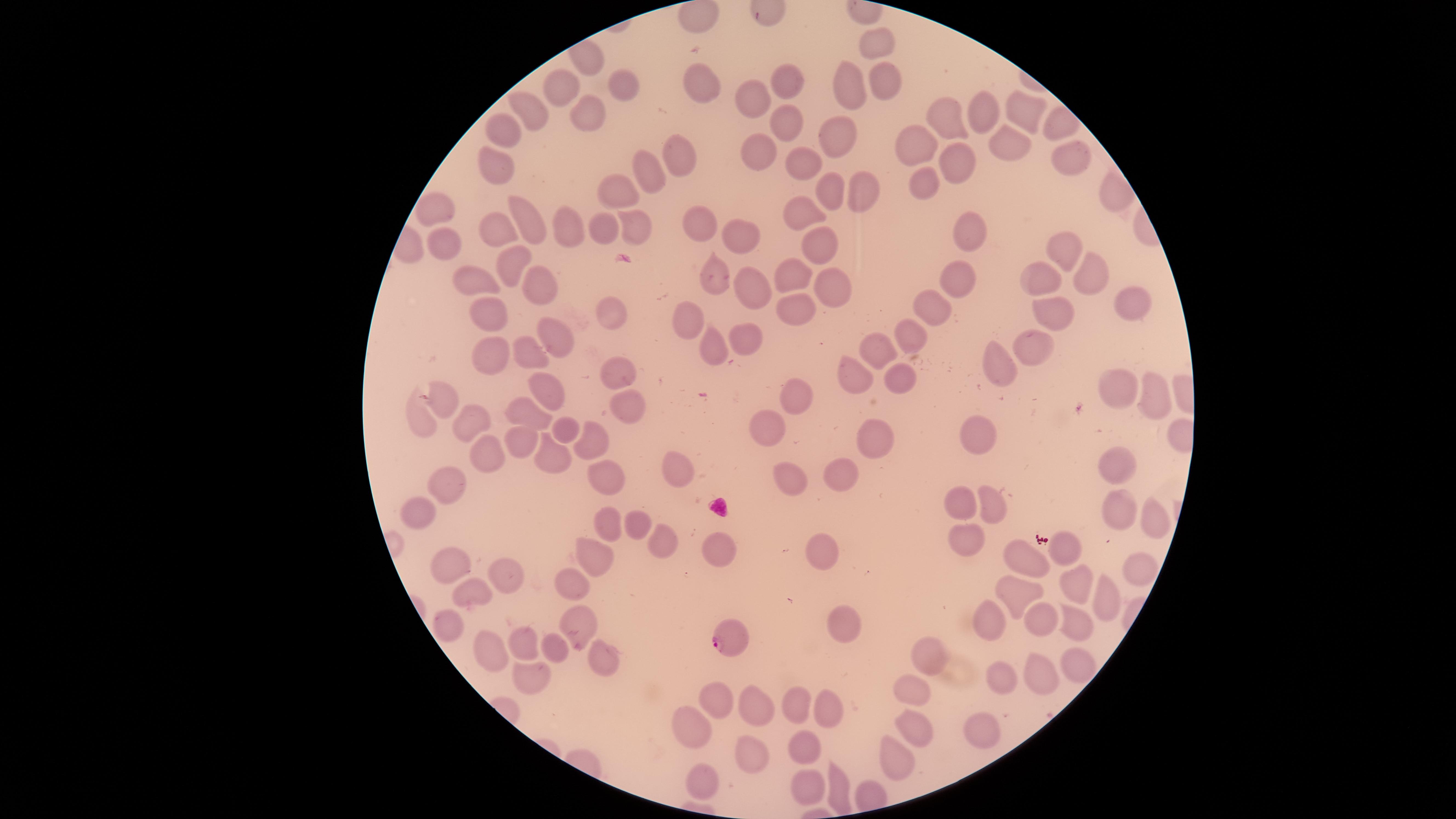
stain = Giemsa
preparation = thin blood film
parasitized red blood cells = approximate marker points, in pixels from the top-left corner: (x=734, y=638)
visible region = circular
capture = smartphone photograph through the microscope eyepiece
field of view = single
presence = malaria parasites identified
species = Plasmodium falciparum
uninfected red blood cells = approximate marker points, in pixels from the top-left corner: (x=701, y=14), (x=880, y=36), (x=789, y=76), (x=882, y=79), (x=570, y=80), (x=703, y=83), (x=849, y=83), (x=626, y=84), (x=750, y=100), (x=535, y=104), (x=581, y=111), (x=986, y=111), (x=1030, y=112), (x=957, y=118), (x=783, y=126), (x=506, y=129), (x=835, y=132), (x=915, y=142), (x=1004, y=143), (x=684, y=152), (x=758, y=152), (x=799, y=156), (x=493, y=158), (x=953, y=165), (x=649, y=176), (x=921, y=179), (x=825, y=185), (x=860, y=185), (x=616, y=192), (x=436, y=202), (x=805, y=210), (x=528, y=212), (x=702, y=223), (x=570, y=224), (x=602, y=229), (x=631, y=231), (x=500, y=234), (x=739, y=236), (x=976, y=236), (x=444, y=237), (x=1063, y=244), (x=819, y=245), (x=508, y=260), (x=1086, y=265), (x=713, y=267), (x=791, y=273), (x=484, y=278), (x=965, y=278), (x=1046, y=279), (x=830, y=281), (x=535, y=286), (x=748, y=292), (x=1132, y=306), (x=793, y=307), (x=611, y=309), (x=936, y=310), (x=1052, y=315), (x=495, y=318), (x=693, y=323), (x=912, y=333), (x=743, y=335), (x=555, y=338), (x=1031, y=341), (x=879, y=344), (x=531, y=348), (x=717, y=348), (x=489, y=358), (x=993, y=365), (x=897, y=371), (x=621, y=375), (x=857, y=375), (x=547, y=386), (x=1119, y=386), (x=796, y=388), (x=443, y=390), (x=1157, y=395), (x=625, y=408), (x=424, y=412), (x=533, y=415), (x=471, y=428), (x=569, y=428), (x=766, y=428), (x=594, y=429), (x=973, y=431), (x=874, y=433), (x=523, y=443), (x=548, y=453), (x=484, y=458), (x=1114, y=467), (x=603, y=470), (x=674, y=470), (x=840, y=470), (x=783, y=478), (x=447, y=489), (x=962, y=502), (x=987, y=502), (x=414, y=509), (x=1118, y=509), (x=1148, y=518), (x=608, y=519), (x=635, y=525), (x=713, y=539), (x=964, y=544), (x=662, y=546), (x=821, y=547), (x=1075, y=548), (x=1030, y=551), (x=595, y=552), (x=448, y=562), (x=1134, y=568), (x=1078, y=578), (x=578, y=580), (x=507, y=582), (x=1098, y=590), (x=1011, y=592), (x=474, y=599), (x=1032, y=614), (x=995, y=615), (x=443, y=620), (x=845, y=622), (x=574, y=623), (x=1071, y=623), (x=529, y=643), (x=554, y=646), (x=924, y=648), (x=494, y=652), (x=599, y=658), (x=1065, y=660), (x=1031, y=670), (x=999, y=674), (x=533, y=675), (x=914, y=694), (x=715, y=697), (x=800, y=702), (x=760, y=705), (x=826, y=706), (x=690, y=715), (x=910, y=724), (x=978, y=729), (x=806, y=739), (x=745, y=752), (x=894, y=757), (x=703, y=777), (x=808, y=782), (x=837, y=784)
image size = 1456×819 pixels